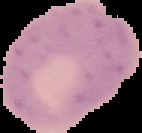

{
  "preparation": "thin blood film",
  "image_type": "cell region segmented out of the field of view; surrounding area masked to black",
  "image_size": "142×133 pixels",
  "result": "no Plasmodium parasites seen"
}